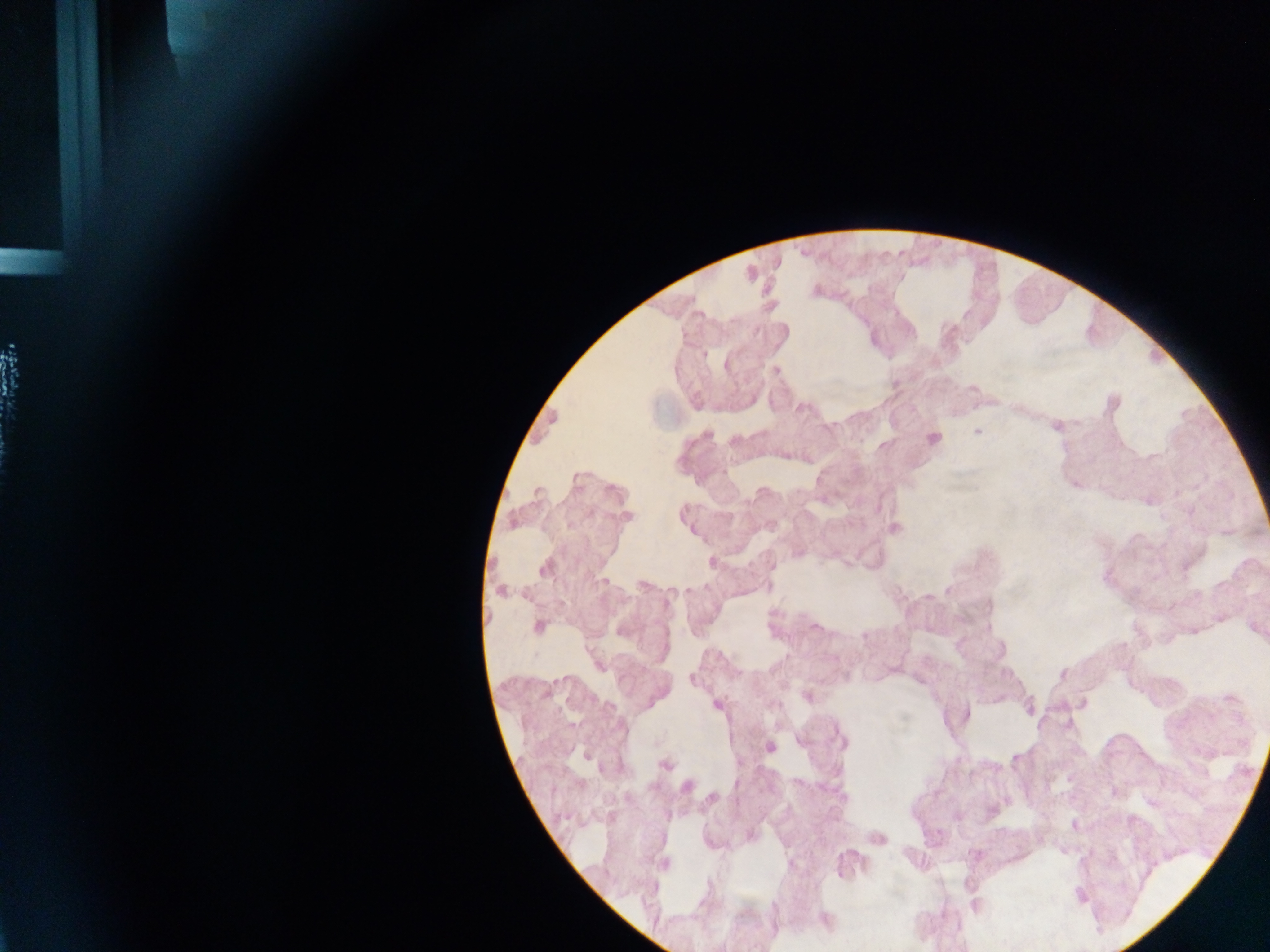

Approximate centers as {x, y} in pixels. Plasmodium parasite locations: {776, 370}, {978, 431}, {934, 438}, {628, 516}, {894, 529}, {544, 570}, {500, 592}, {538, 626}, {691, 678}, {665, 765}, {687, 786}. Mobile-phone photograph taken through the microscope. Collected in Ghana. Thick blood film. Image is 1270×952 pixels. Single field of view.